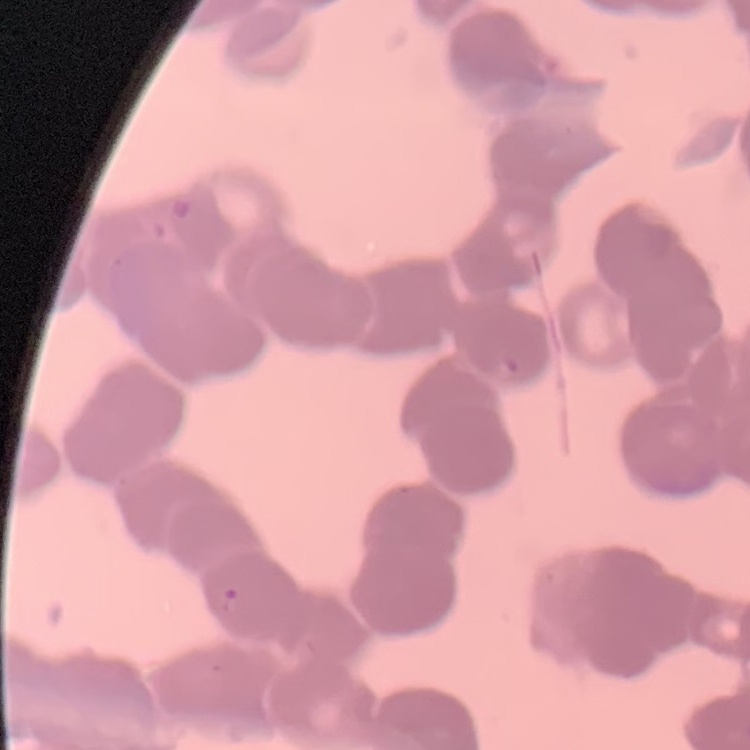
red blood cell morphology = rouleaux formation
image type = one tile cut from a larger photomicrograph
stain = Field's or Giemsa
preparation = thin peripheral smear